Give the position of every malaria parasite and every leukocyte.
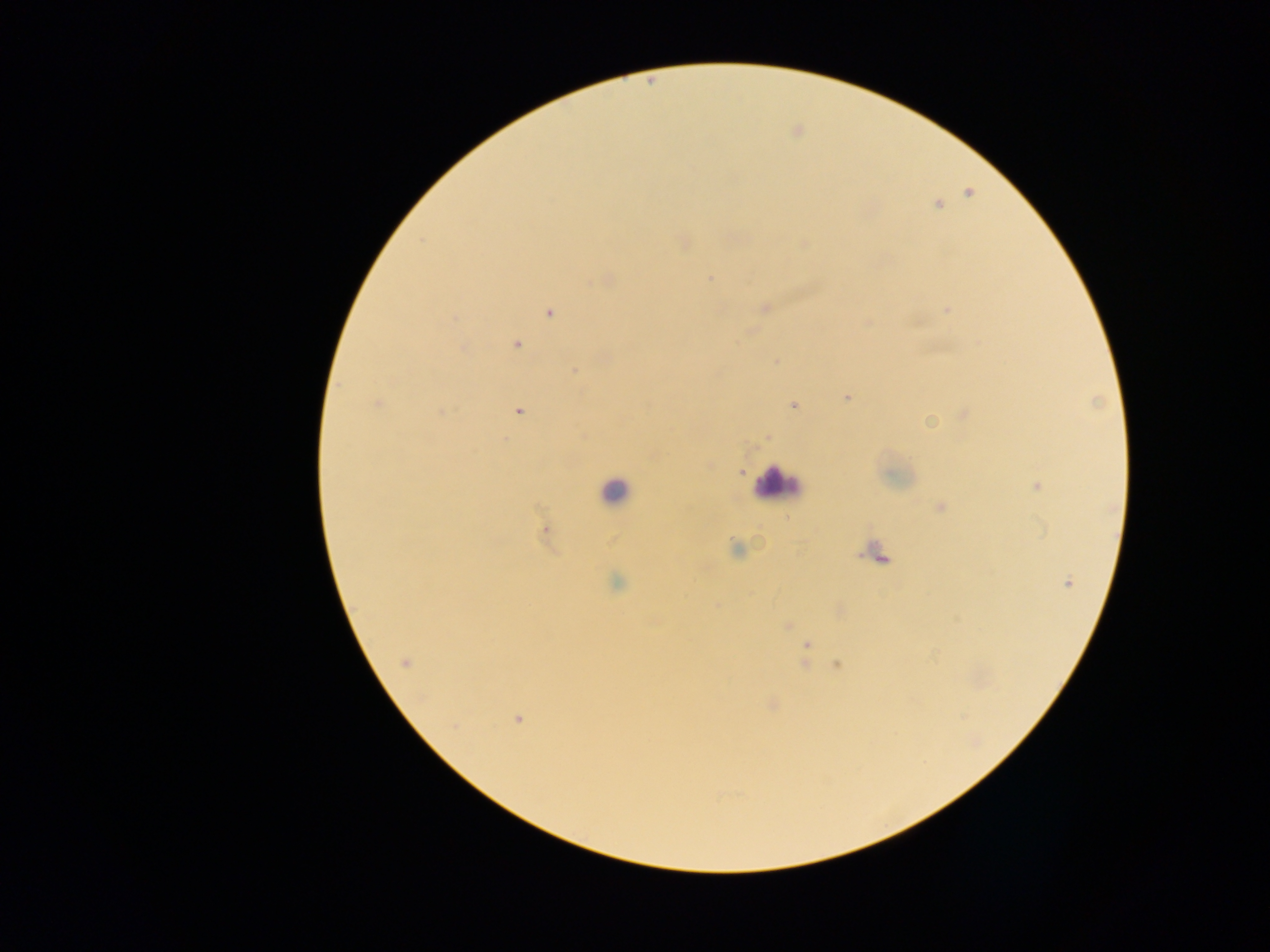
Approximate centers as {x, y} in pixels.
Malaria parasites: {968, 193}, {938, 204}, {683, 242}, {803, 244}, {709, 278}, {605, 280}, {764, 307}, {947, 309}, {549, 312}, {516, 345}, {462, 347}, {776, 360}, {574, 370}, {847, 398}, {377, 403}, {793, 405}, {517, 410}, {963, 412}, {930, 422}, {766, 437}, {739, 471}, {1037, 486}, {940, 507}, {546, 532}, {736, 548}, {879, 556}, {1067, 582}, {616, 583}, {717, 605}, {839, 610}, {787, 626}, {806, 644}, {405, 662}, {805, 662}, {837, 664}, {772, 704}, {518, 717}.
Leukocytes: {777, 483}, {615, 491}.

One field of view. Photographed through a microscope with a mobile-phone camera. Image is 1270×952 pixels. Sample from Ghana. Thick blood smear.